Locate and identify every blood parasite.
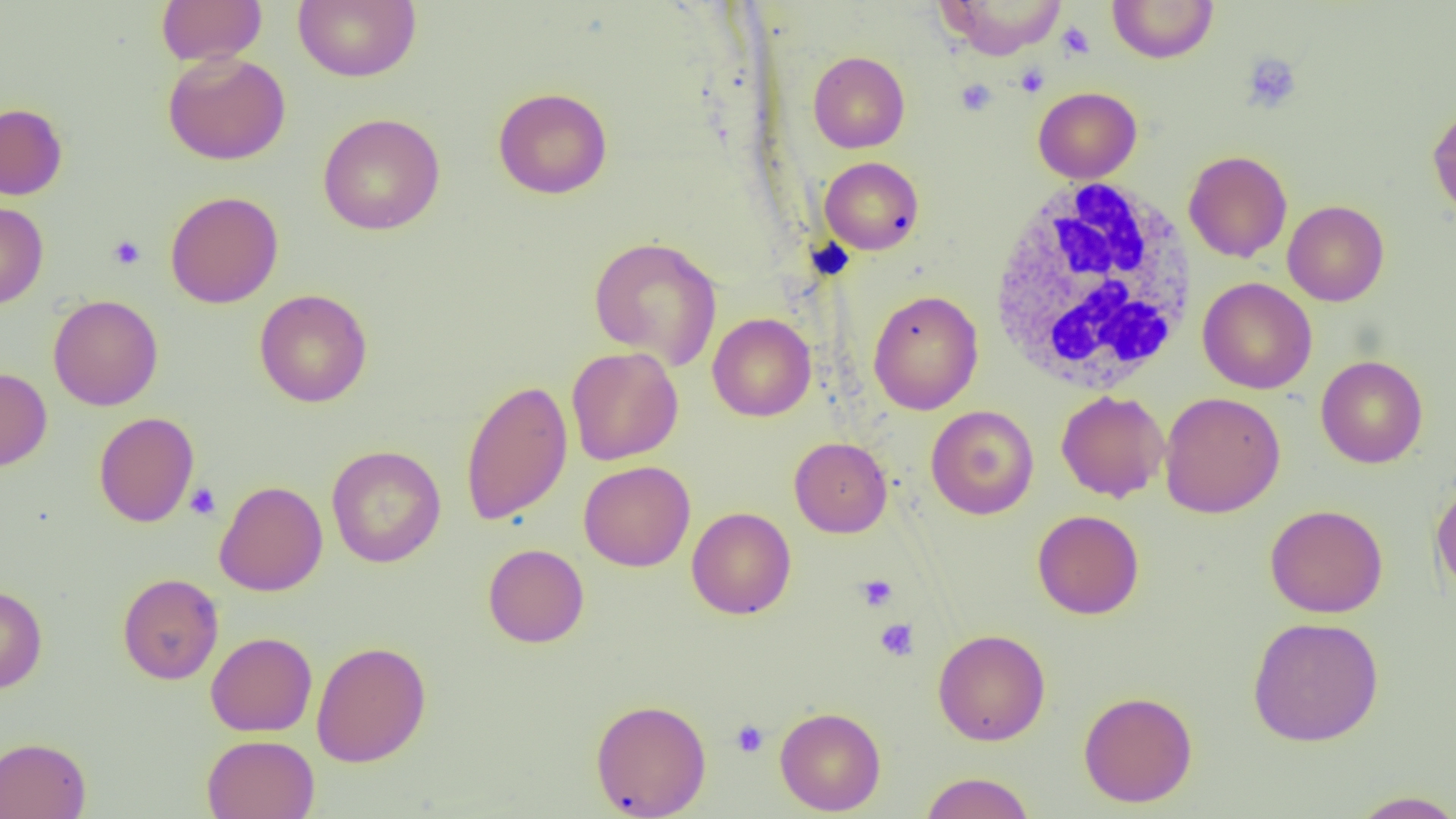
No blood parasites observed.

Summary:
  - Coordinate format: approximate bounding boxes as (x1,y1)-(x2,y2) corner pairs in pixels
  - White blood cell locations: (987,176)-(1201,395)
  - Uninfected red blood cell locations: (156,0)-(268,66), (292,0)-(421,83), (938,0)-(1068,59), (1107,0)-(1219,63), (162,51)-(291,165), (808,51)-(909,153), (1033,86)-(1142,183), (493,87)-(612,199), (0,102)-(67,200), (1427,103)-(1456,223), (318,112)-(445,235), (1183,150)-(1292,263), (819,156)-(924,255), (165,191)-(283,308), (1282,200)-(1389,306), (0,201)-(48,309), (589,236)-(722,369), (1198,277)-(1317,394), (254,288)-(372,407), (868,289)-(983,415), (48,294)-(163,411), (707,313)-(816,421), (566,346)-(682,465), (1316,355)-(1428,468), (0,367)-(52,470), (460,378)-(573,525), (1056,390)-(1169,502), (1159,391)-(1286,519), (925,405)-(1039,519), (94,411)-(199,527), (789,436)-(892,538), (326,445)-(446,568), (578,460)-(695,571), (1431,479)-(1456,599), (214,480)-(328,596), (1265,503)-(1388,618), (687,506)-(796,619), (1032,509)-(1144,619), (483,543)-(589,647), (117,573)-(223,684), (0,584)-(47,694), (1247,616)-(1384,747), (933,628)-(1050,745), (205,631)-(317,736), (311,640)-(432,767), (1078,690)-(1198,807), (590,698)-(712,818), (774,706)-(886,816), (202,734)-(320,819), (0,736)-(91,819), (919,772)-(1035,819), (1348,789)-(1456,818)
  - Platelet locations: (1057,22)-(1095,59), (1241,52)-(1302,113), (1015,63)-(1049,97), (955,79)-(997,115), (108,234)-(145,270), (185,482)-(221,520), (856,574)-(898,612), (875,618)-(919,661), (731,719)-(769,758)
  - Slide-level diagnosis: no evidence of blood parasites
  - Field of view: single
  - Image size: 1456×819 pixels
  - Modality: light microscopy
  - Preparation: thin blood film
  - Magnification: 1000x